Identify the parasite.
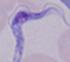
This is a trypanosome.

1000x magnification. Micrograph.